Assess this cell for malaria.
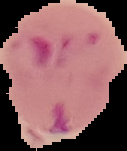
Parasitized.

image type = segmented cell region on a black background
preparation = thin blood film
image size = 127×151 pixels